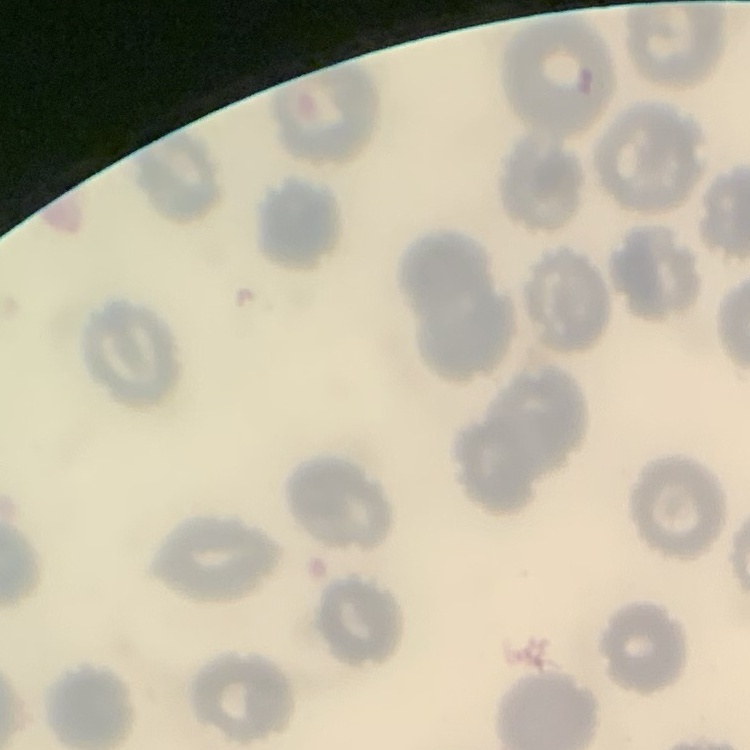
The red blood cells show no rouleaux formation. Stained with either Field's or Giemsa. One tile cut from a larger photomicrograph. Thin peripheral smear.